Identify the parasite.
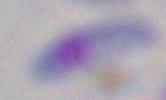

This is Toxoplasma gondii.

modality = micrograph
magnification = 1000x